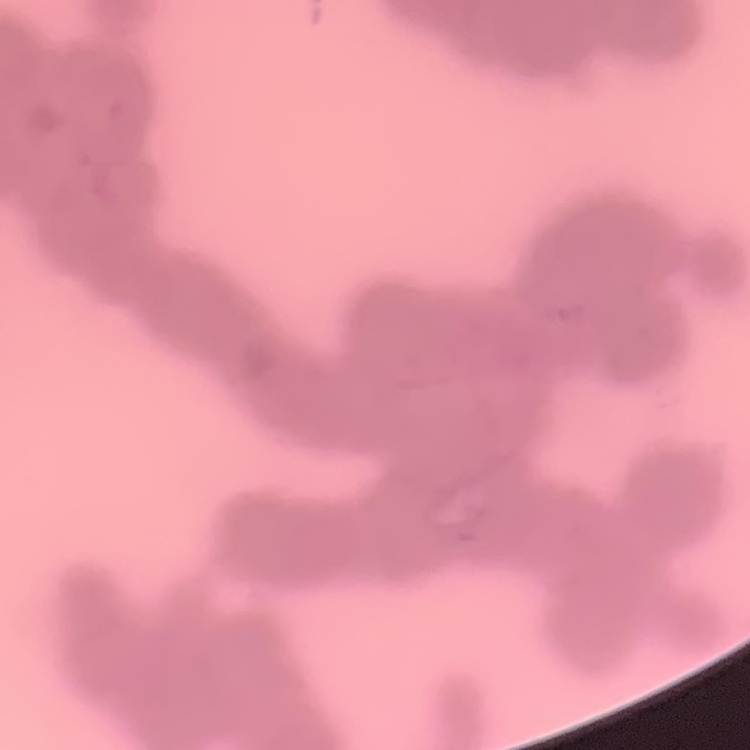

{
  "red_blood_cell_morphology": "rouleaux formation",
  "stain": "Field's or Giemsa",
  "image_type": "one tile cut from a larger photomicrograph",
  "preparation": "thin blood film"
}